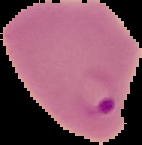

Summary:
  - Image size: 142×145 pixels
  - Result: malaria parasites identified
  - Image type: segmented cell region with the area outside set to black
  - Preparation: thin blood smear